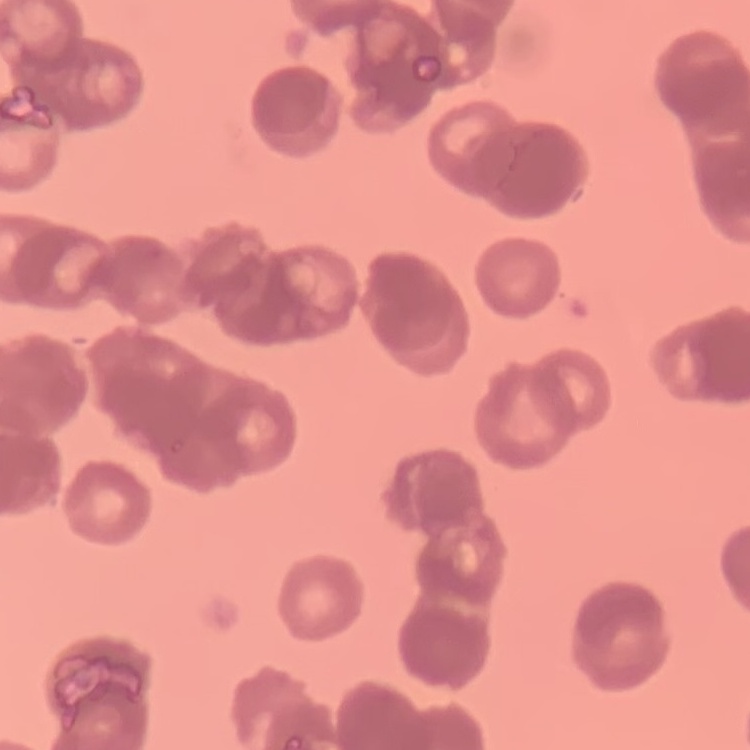

Summary:
  - Erythrocyte morphology: rouleaux formation
  - Image type: square crop of a larger photomicrograph
  - Stain: Field's or Giemsa
  - Preparation: thin peripheral smear